Give a bounding box for every artifact (stain precipitate or debris).
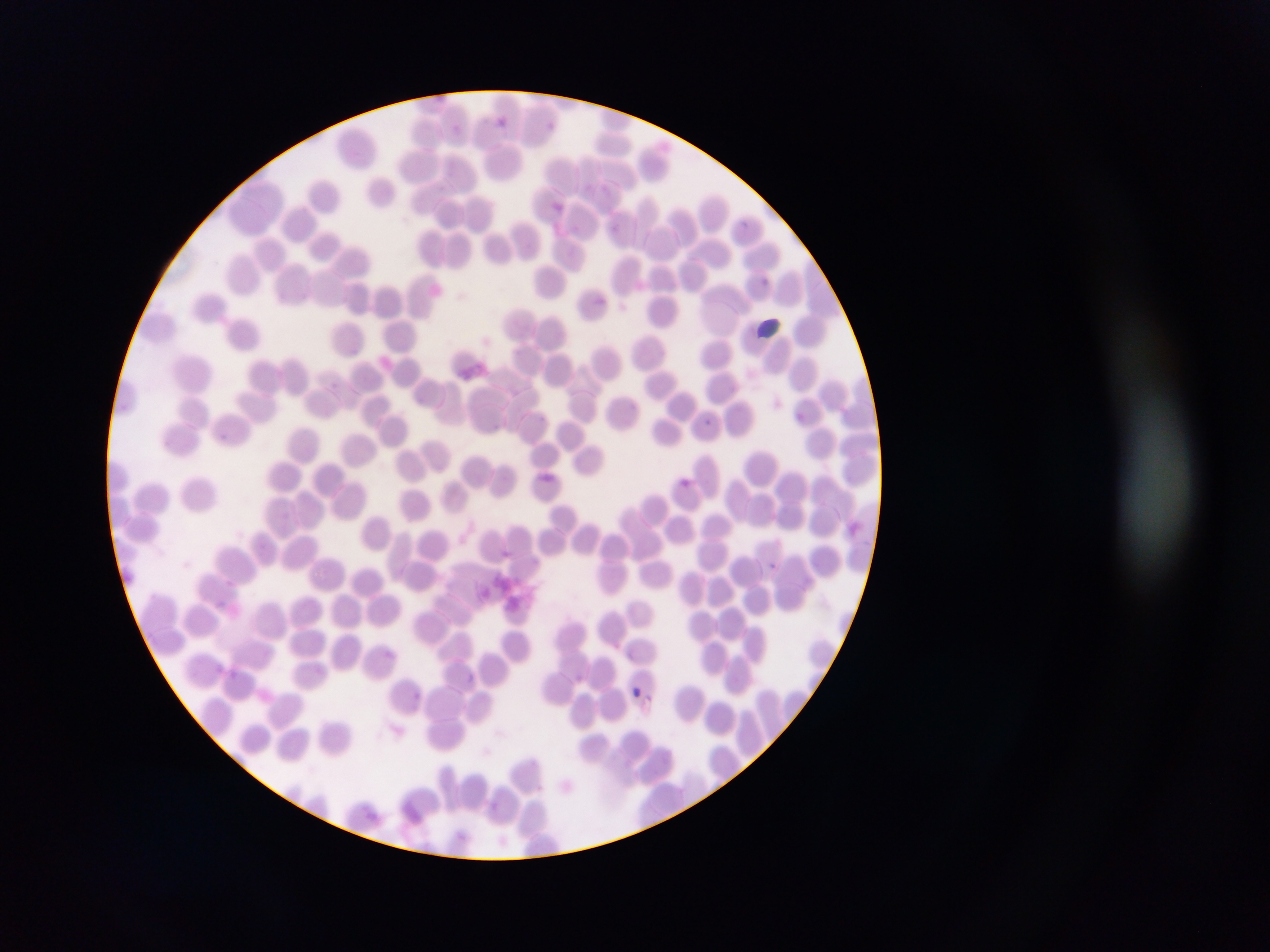
Approximate bounding boxes as left top right bottom in pixels.
Artifacts (stain precipitate or debris): 478 570 574 620.

Summary:
  - Plasmodium parasite locations: 549 199 564 212; 762 278 770 285; 754 315 789 343; 795 411 803 424; 705 419 715 429; 680 475 696 489; 766 561 780 575; 215 598 229 608; 227 667 242 681; 626 685 650 707; 409 689 424 704
  - Country: Ghana
  - Capture: mobile-phone photograph through a microscope
  - Image size: 1270×952 pixels
  - Preparation: thin blood smear
  - Field of view: single